Outline each blood parasite and name the species.
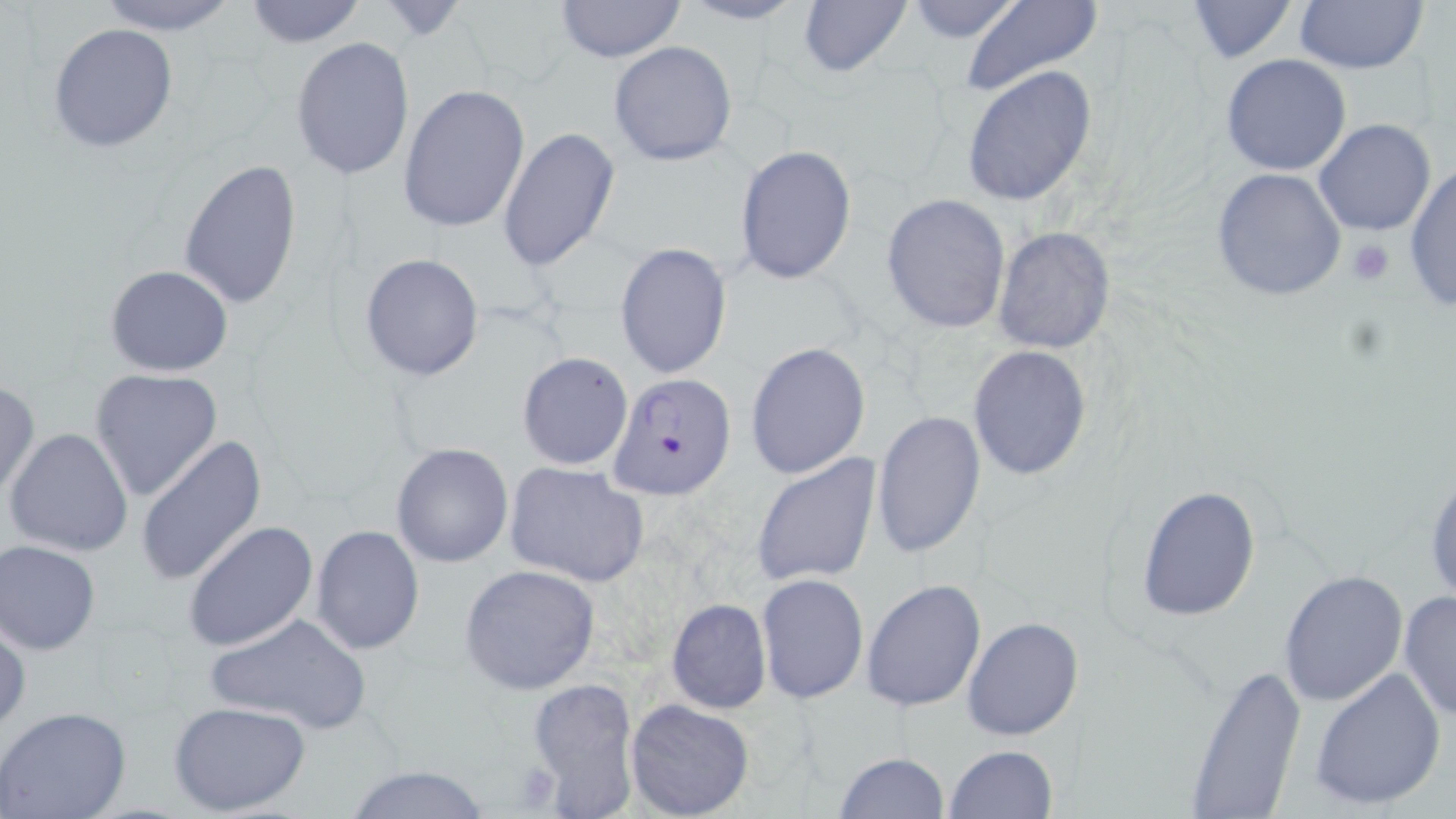
Approximate bounding boxes as [x1, y1, x2, y2] in pixels.
Plasmodium falciparum-infected red blood cells: [608, 373, 736, 500].
No Plasmodium ovale, Plasmodium malariae, Plasmodium vivax, Babesia divergens, or Trypanosoma brucei observed.

Uninfected red blood cell locations: [92, 0, 244, 36], [241, 0, 369, 49], [554, 0, 686, 63], [799, 0, 912, 77], [902, 0, 1025, 43], [958, 0, 1104, 97], [1187, 0, 1298, 62], [1294, 0, 1426, 73], [678, 1, 811, 26], [48, 22, 179, 154], [291, 36, 415, 181], [607, 42, 738, 167], [1220, 54, 1351, 176], [961, 67, 1098, 208], [399, 84, 531, 234], [1315, 119, 1437, 237], [498, 127, 621, 271], [734, 143, 857, 286], [179, 159, 303, 311], [1405, 162, 1456, 312], [1211, 167, 1347, 302], [880, 193, 1011, 334], [993, 226, 1114, 356], [614, 242, 733, 380], [360, 253, 485, 381], [104, 264, 233, 377], [746, 342, 872, 478], [967, 345, 1092, 481], [516, 351, 634, 470], [88, 367, 224, 503], [0, 378, 39, 500], [872, 410, 986, 558], [5, 427, 131, 559], [137, 436, 266, 586], [391, 442, 512, 568], [752, 452, 881, 586], [503, 461, 650, 588], [1425, 464, 1456, 608], [1134, 483, 1263, 622], [183, 521, 318, 652], [310, 524, 424, 656], [1, 540, 101, 655], [460, 563, 600, 694], [1277, 569, 1408, 707], [757, 573, 868, 703], [861, 579, 986, 711], [1398, 592, 1455, 723], [664, 599, 773, 715], [203, 613, 373, 736], [962, 615, 1084, 742], [0, 616, 29, 734], [1183, 662, 1307, 818], [1309, 666, 1446, 809], [526, 675, 641, 816], [625, 698, 754, 819], [169, 700, 312, 816], [0, 708, 131, 819], [943, 745, 1057, 819], [834, 752, 949, 819], [343, 764, 493, 819]. Platelet locations: [1346, 238, 1395, 289], [511, 759, 562, 812]. Slide-level diagnosis: Plasmodium falciparum. One field of a larger specimen. Thin blood film. May-Grünwald-Giemsa-stained preparation. Light microscopy. Image is 1456×819 pixels. 1000x magnification.